Comment on the morphology of the erythrocytes.
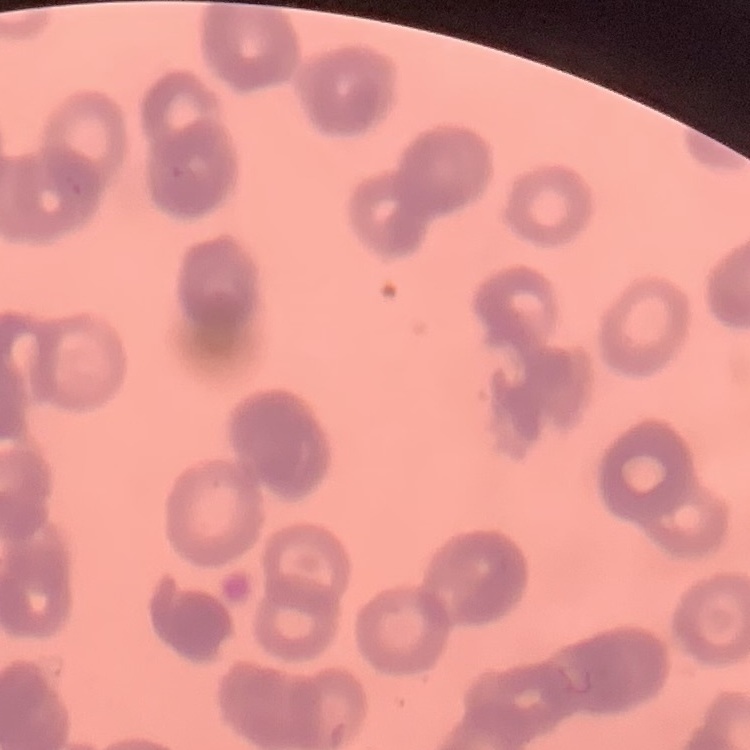
Rouleaux formation.

Stained with either Field's or Giemsa. Square crop of a larger photomicrograph. Thin peripheral smear.